Assess this cell for malaria.
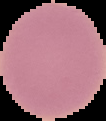

Uninfected.

Image is 106×121 pixels. From a thin blood smear. The area outside the segmented cell region is set to black.